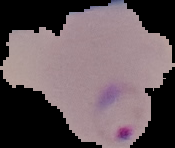 Segmented cell region on a black background. Result: malaria parasites identified. Image is 175×148 pixels. From a thin blood film.